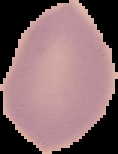 Image is 118×154 pixels. From a thin blood smear. Malaria status: uninfected. Cell region segmented out of the field of view; the surrounding area is masked to black.